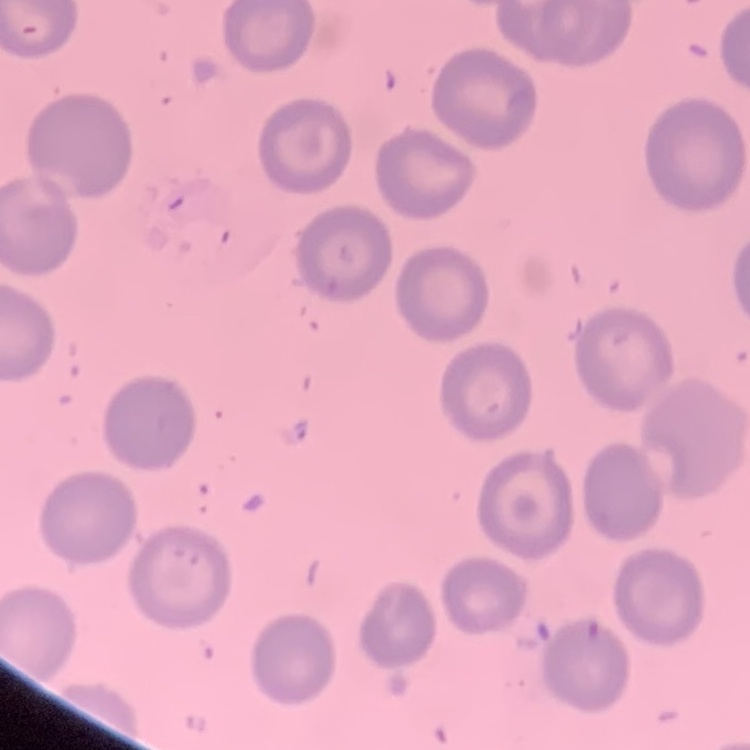
The erythrocytes show no rouleaux formation. Stained with either Field's or Giemsa. One tile cut from a larger photomicrograph. Thin peripheral smear.